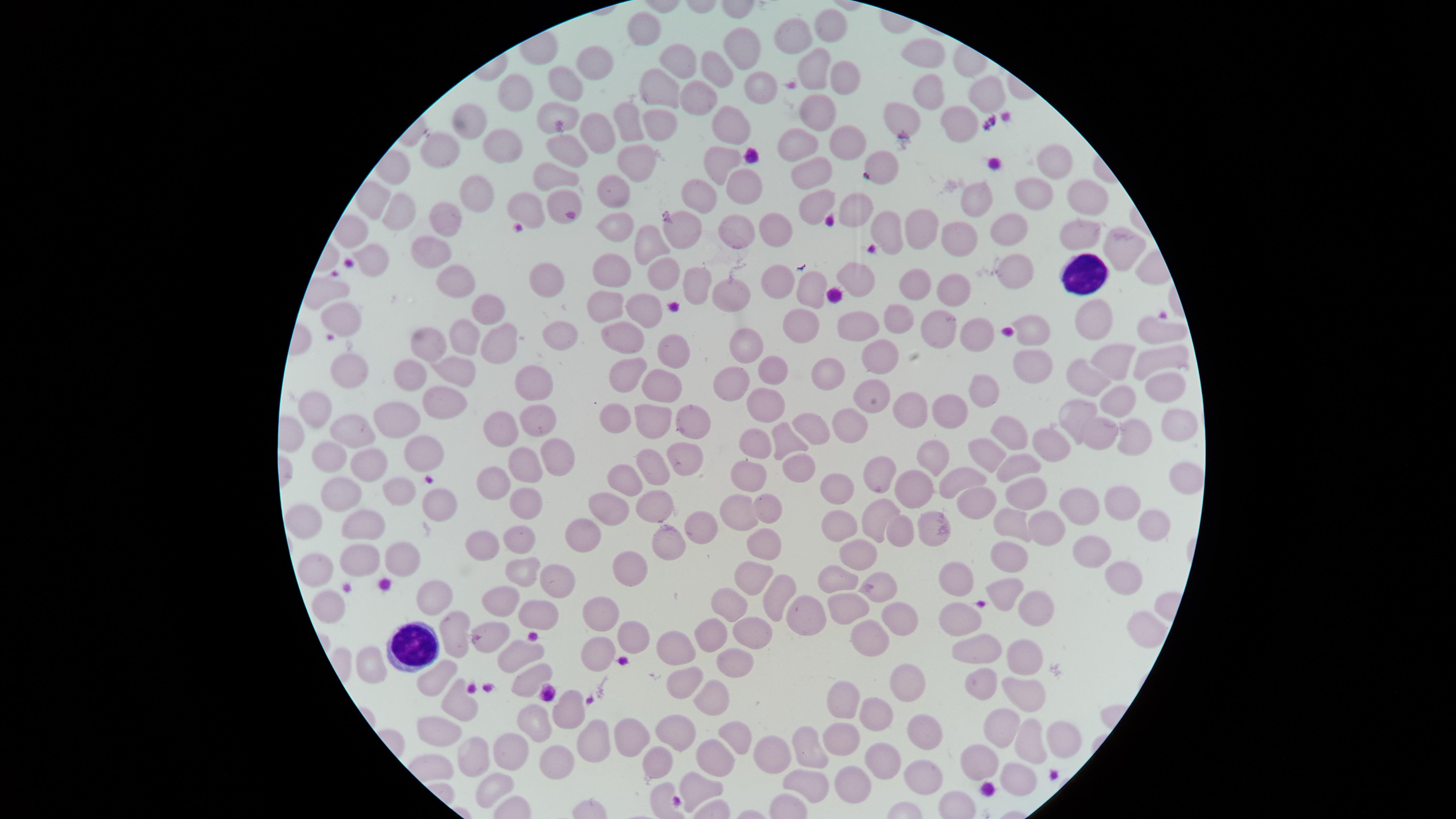

preparation = thin smear of blood
presence = no malaria parasites identified
capture = smartphone photograph through the microscope eyepiece
uninfected red blood cells = approximate marker points as {x, y} in pixels: {646, 27}, {827, 27}, {795, 32}, {741, 49}, {923, 50}, {683, 62}, {591, 64}, {814, 65}, {714, 69}, {844, 73}, {562, 80}, {659, 86}, {759, 86}, {521, 89}, {925, 89}, {986, 91}, {698, 96}, {549, 111}, {819, 113}, {660, 119}, {479, 121}, {901, 121}, {628, 122}, {959, 123}, {733, 127}, {598, 133}, {843, 139}, {794, 143}, {443, 148}, {508, 148}, {564, 148}, {1053, 162}, {636, 164}, {880, 164}, {724, 166}, {815, 177}, {555, 178}, {744, 183}, {484, 193}, {695, 193}, {1081, 194}, {616, 195}, {1031, 195}, {815, 203}, {860, 203}, {401, 205}, {531, 205}, {977, 205}, {441, 207}, {558, 207}, {884, 223}, {769, 224}, {1004, 227}, {736, 228}, {1072, 228}, {679, 229}, {924, 229}, {617, 230}, {957, 235}, {645, 244}, {1115, 248}, {428, 254}, {375, 264}, {660, 271}, {1014, 272}, {548, 273}, {609, 273}, {863, 274}, {772, 275}, {452, 276}, {919, 279}, {695, 282}, {730, 288}, {951, 290}, {811, 291}, {603, 308}, {484, 311}, {640, 312}, {1089, 315}, {901, 317}, {342, 318}, {937, 325}, {801, 327}, {1030, 328}, {558, 329}, {974, 330}, {1150, 331}, {855, 333}, {458, 335}, {626, 335}, {428, 340}, {747, 344}, {668, 348}, {499, 351}, {878, 355}, {1159, 359}, {1030, 365}, {1112, 365}, {346, 366}, {767, 370}, {409, 371}, {456, 371}, {831, 372}, {730, 373}, {623, 374}, {668, 378}, {1089, 378}, {1156, 384}, {537, 386}, {985, 394}, {435, 401}, {874, 402}, {312, 404}, {760, 406}, {1120, 408}, {402, 409}, {958, 409}, {1074, 413}, {908, 417}, {659, 420}, {611, 421}, {539, 422}, {1173, 422}, {689, 424}, {815, 424}, {855, 429}, {495, 431}, {363, 432}, {1014, 432}, {1096, 433}, {786, 438}, {1134, 438}, {751, 439}, {1052, 443}, {417, 450}, {679, 453}, {982, 453}, {936, 454}, {324, 455}, {551, 459}, {649, 459}, {516, 462}, {1019, 463}, {361, 465}, {802, 469}, {883, 469}, {962, 477}, {625, 478}, {1179, 479}, {489, 481}, {752, 481}, {917, 491}, {1028, 492}, {401, 493}, {837, 493}, {340, 494}, {656, 501}, {968, 501}, {1122, 501}, {1076, 502}, {765, 504}, {529, 505}, {613, 505}, {433, 510}, {734, 512}, {873, 513}, {1009, 517}, {367, 522}, {1150, 522}, {306, 523}, {835, 525}, {937, 526}, {701, 528}, {588, 530}, {1041, 531}, {898, 532}, {518, 537}, {487, 540}, {668, 546}, {767, 548}, {1090, 555}, {857, 556}, {362, 560}, {401, 560}, {1006, 560}, {317, 564}, {522, 569}, {628, 572}, {752, 572}, {556, 576}, {958, 577}, {834, 579}, {875, 580}, {1116, 580}, {1009, 589}, {773, 594}, {437, 600}, {503, 602}, {327, 604}, {730, 604}, {1028, 605}, {844, 609}, {539, 612}, {795, 613}, {602, 615}, {896, 617}, {957, 619}, {1138, 626}, {452, 628}, {714, 634}, {762, 634}, {631, 636}, {487, 638}, {671, 643}, {873, 643}, {518, 647}, {975, 649}, {600, 653}, {1021, 658}, {733, 660}, {526, 673}, {682, 680}, {432, 684}, {900, 684}, {983, 687}, {714, 694}, {1022, 694}, {840, 699}, {460, 705}, {567, 708}, {875, 715}, {536, 720}, {1004, 725}, {631, 730}, {670, 731}, {431, 732}, {918, 734}, {837, 737}, {1055, 737}, {590, 741}, {727, 745}, {1028, 745}, {808, 747}, {654, 753}, {885, 754}, {513, 755}, {555, 758}, {712, 759}, {477, 760}, {773, 760}, {976, 764}, {920, 774}, {851, 780}, {1014, 780}, {805, 782}, {695, 783}, {485, 789}
stain = Giemsa
field of view = single
image size = 1456×819 pixels
white blood cells = approximate marker points as {x, y} in pixels: {1080, 275}, {416, 644}
visible region = circular